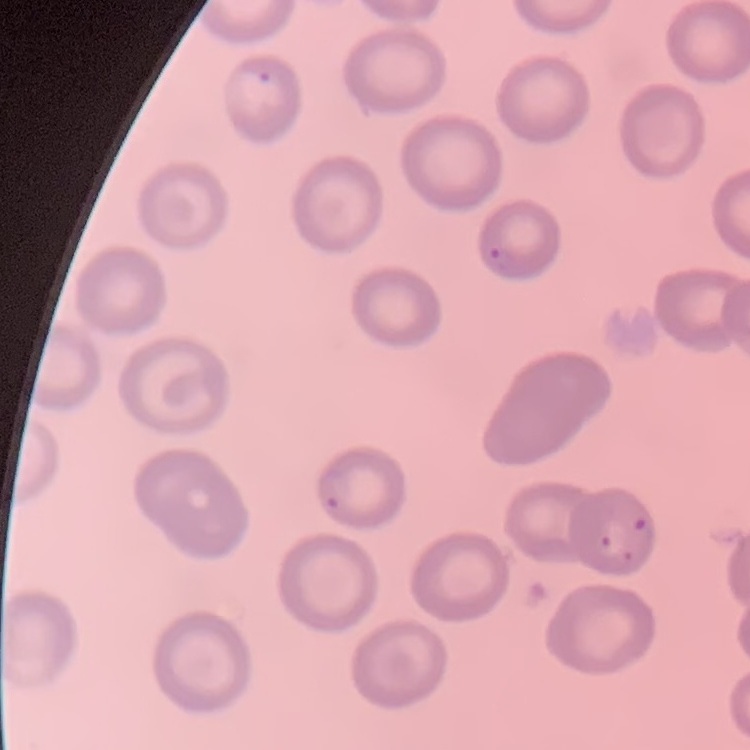

erythrocyte_morphology: no rouleaux formation
image_type: square crop of a larger photomicrograph
stain: Field's or Giemsa
preparation: thin blood smear